Point out leukocytes.
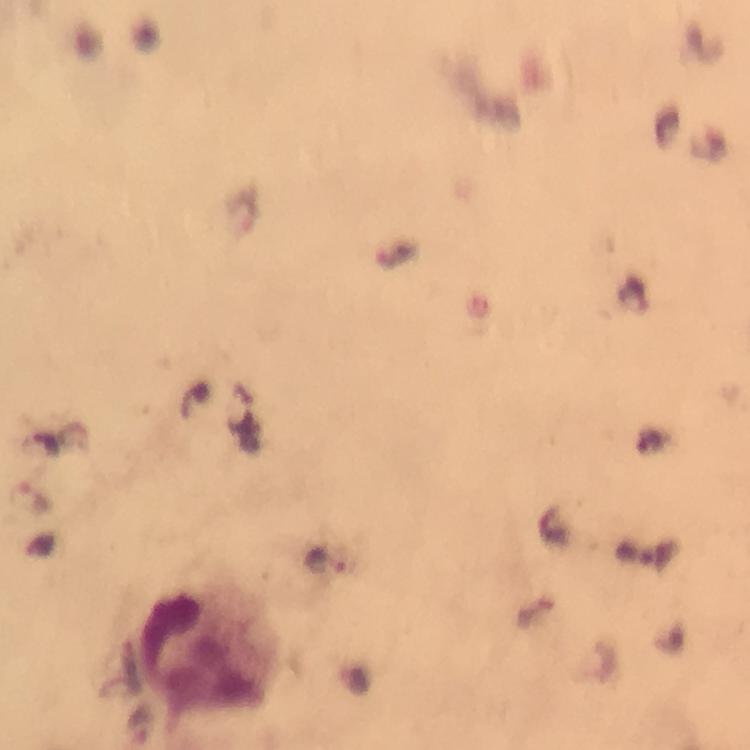

Approximate centers as (x, y) in pixels.
Leukocytes: (200, 658).

Malaria parasite locations: (241, 209), (326, 559). Immersion oil applied. Giemsa stain. Smartphone photograph taken through a microscope. Thick blood film. From a malaria diagnostic workup. Cropped region of a single field of view. Image is 750×750 pixels. 100x magnification.